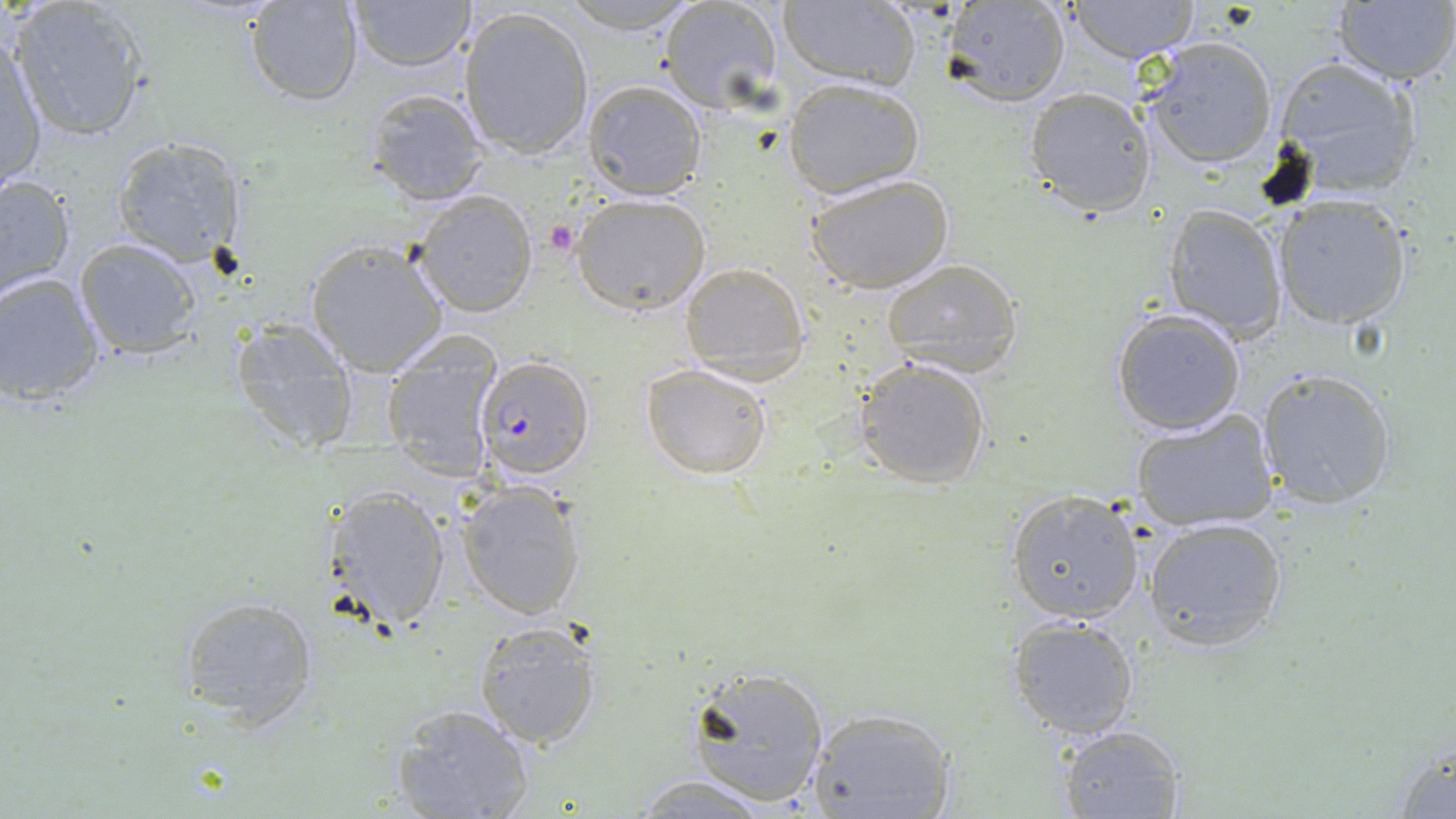
Summary:
  - Coordinate format: approximate bounding boxes as (x1,y1)-(x2,y2) corner pairs in pixels
  - Platelet locations: (542,221)-(578,257)
  - Uninfected red blood cell locations: (8,0)-(153,141), (347,0)-(476,73), (557,0)-(700,33), (1332,0)-(1456,85), (244,1)-(362,107), (1067,1)-(1201,61), (657,2)-(785,112), (776,2)-(920,90), (943,2)-(1071,107), (458,5)-(595,160), (1144,36)-(1280,169), (1,39)-(47,193), (1272,56)-(1426,199), (783,78)-(924,198), (583,79)-(708,201), (1025,87)-(1157,216), (361,90)-(493,207), (110,134)-(247,267), (806,174)-(956,294), (0,175)-(75,301), (412,191)-(539,318), (1271,193)-(1414,328), (572,194)-(711,315), (1162,203)-(1288,338), (72,238)-(204,358), (304,239)-(448,377), (881,257)-(1025,377), (679,262)-(810,383), (0,273)-(105,405), (1109,309)-(1245,435), (229,316)-(361,455), (380,332)-(505,479), (854,357)-(992,488), (641,363)-(772,479), (1256,367)-(1398,509), (1131,411)-(1279,532), (455,484)-(588,620), (323,485)-(451,631), (1006,489)-(1145,624), (1143,517)-(1289,651), (179,596)-(321,725), (1007,616)-(1139,740), (473,620)-(602,751), (682,665)-(832,807), (391,704)-(536,819), (807,706)-(955,818), (1057,723)-(1186,818), (1389,735)-(1456,818), (629,773)-(772,817)
  - Plasmodium falciparum-infected red blood cell locations: (479,358)-(597,484)
  - Slide-level diagnosis: Plasmodium falciparum
  - Preparation: thin blood film
  - Modality: optical microscopy
  - Stain: May-Grünwald-Giemsa
  - Image size: 1456×819 pixels
  - Field of view: single
  - Magnification: 1000x